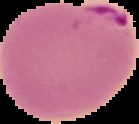

Image is 139×124 pixels. From a thin blood smear. The area outside the segmented cell region is set to black. Result: Plasmodium parasites detected.